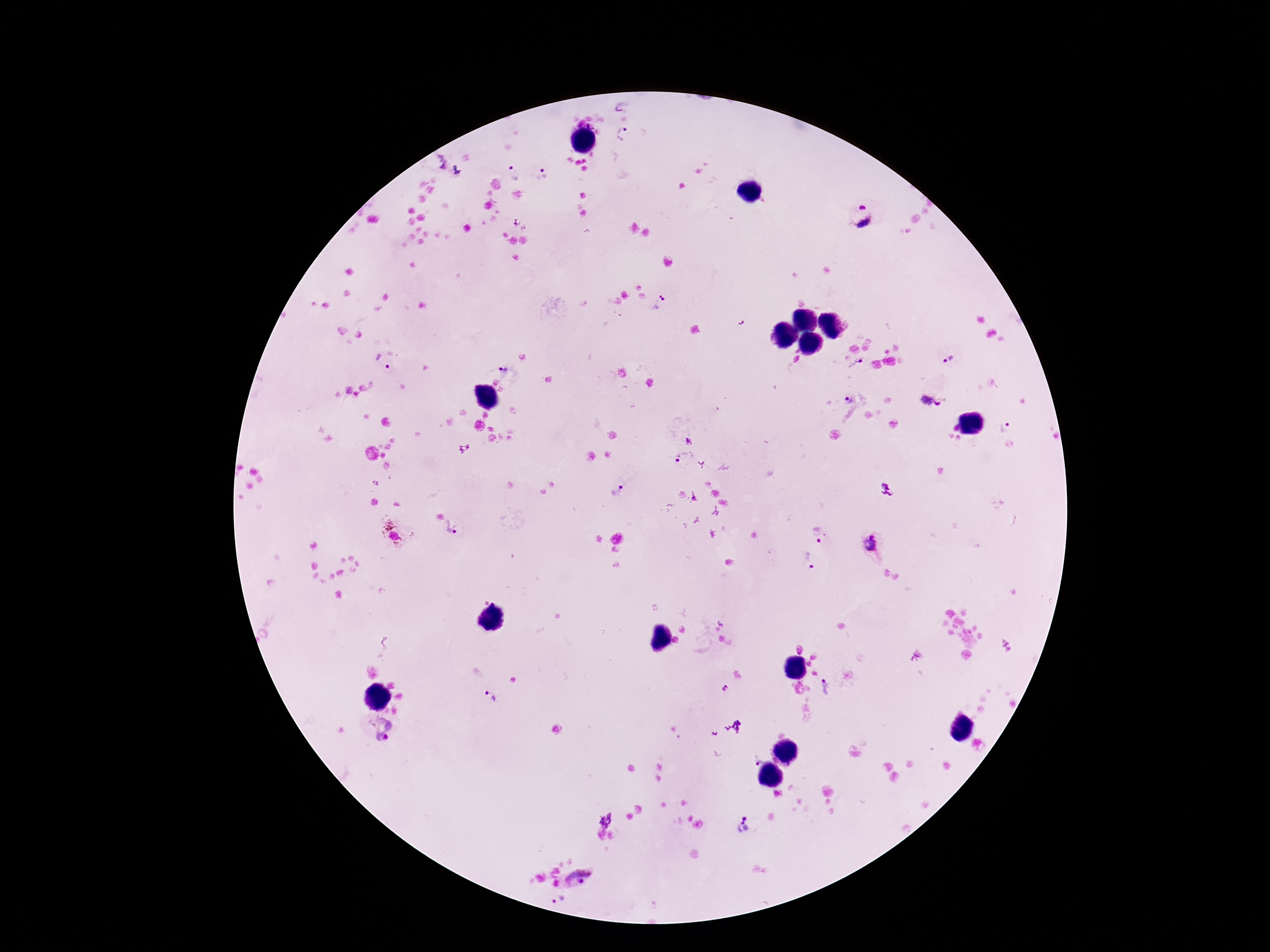

Approximate centers as {x, y} in pixels.
Summary:
  - Plasmodium parasite locations: {624, 105}, {623, 134}, {440, 160}, {456, 171}, {512, 175}, {543, 175}, {860, 217}, {660, 304}, {947, 357}, {380, 365}, {855, 366}, {503, 370}, {848, 400}, {926, 400}, {937, 404}, {1006, 426}, {689, 442}, {686, 455}, {677, 461}, {616, 492}, {453, 530}, {391, 533}, {815, 533}, {868, 543}, {808, 561}, {725, 688}, {825, 688}, {489, 695}, {380, 730}, {755, 759}, {606, 819}, {743, 826}, {581, 878}, {558, 899}
  - Patient malaria status: positive
  - Stain: Giemsa
  - Image size: 1270×952 pixels
  - Magnification: 100x
  - Capture: smartphone camera through the microscope eyepiece
  - Preparation: thick peripheral-blood smear
  - Field of view: one from this slide